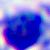
Summary:
  - Magnification: 400x
  - Identification: white blood cell
  - Modality: photomicrograph